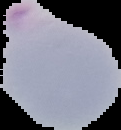

malaria_status: parasitized
preparation: thin blood smear
image_size: 121×130 pixels
image_type: segmented cell region on a black background